Describe the morphology of the erythrocytes.
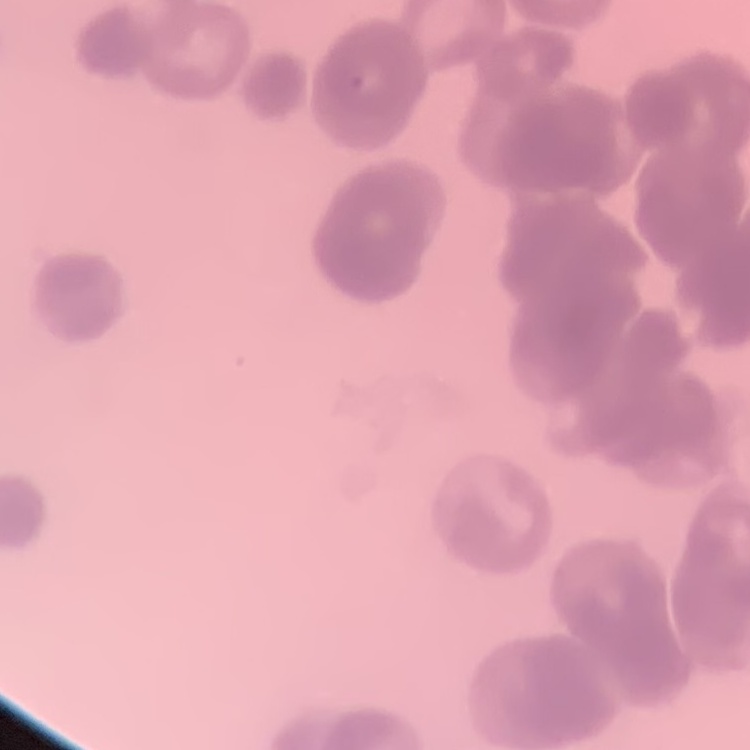

Rouleaux formation.

Square crop of a larger photomicrograph. Stained with either Field's or Giemsa. Thin blood smear.